Outline each Plasmodium falciparum-infected red blood cell.
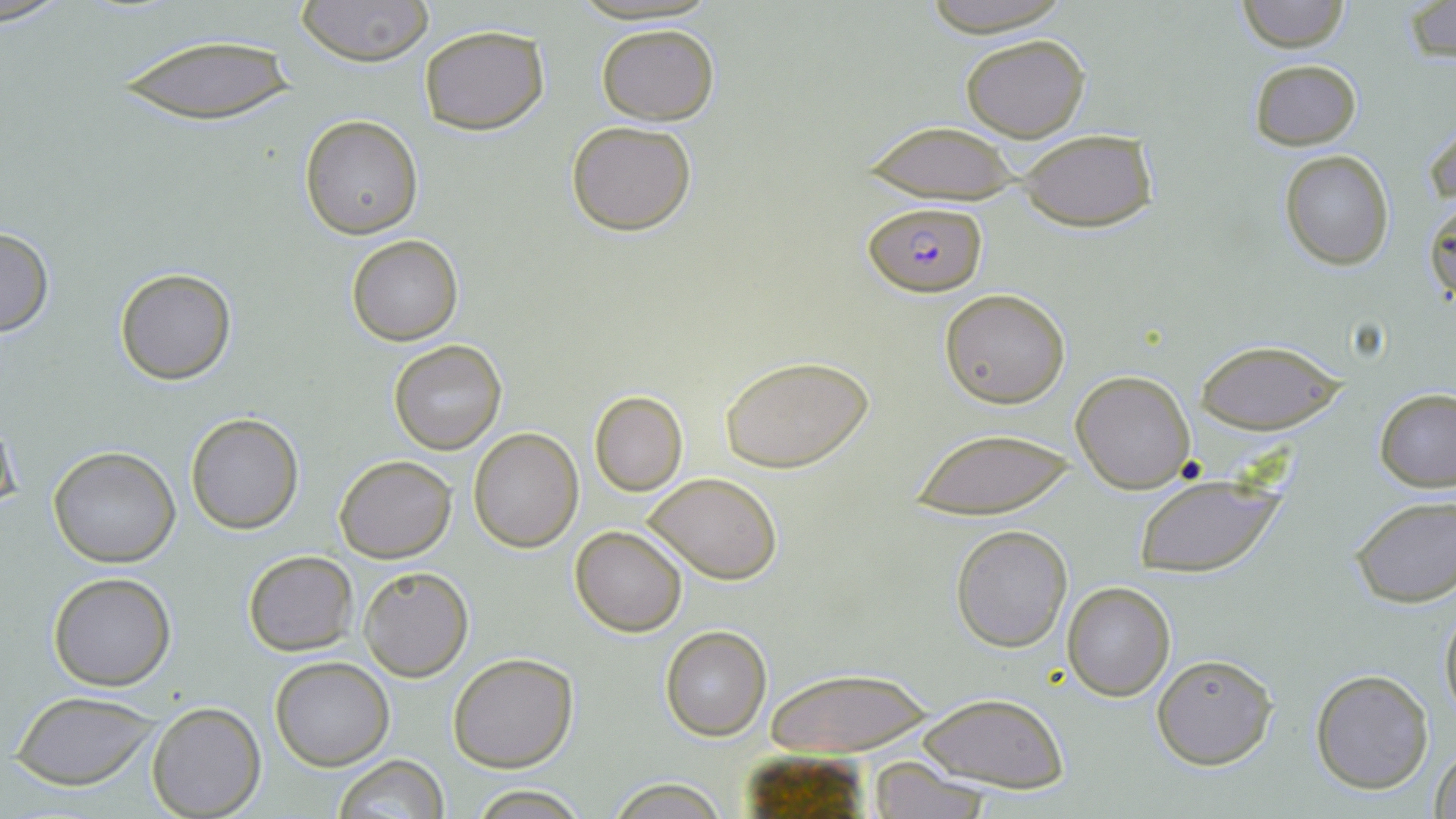

Approximate bounding boxes as (x1, y1, x2, y2) in pixels.
Plasmodium falciparum-infected red blood cells: (864, 200, 985, 295).

Summary:
  - Uninfected red blood cell locations: (295, 0, 432, 66), (1235, 0, 1351, 52), (916, 1, 1074, 35), (1404, 2, 1455, 62), (596, 23, 721, 125), (419, 25, 549, 133), (959, 32, 1093, 142), (116, 34, 300, 124), (1249, 58, 1361, 150), (300, 114, 423, 239), (1425, 120, 1455, 208), (566, 121, 697, 236), (862, 121, 1020, 202), (1015, 129, 1159, 232), (1280, 149, 1396, 271), (1425, 198, 1455, 311), (0, 227, 53, 339), (347, 236, 462, 346), (114, 268, 235, 385), (939, 288, 1071, 408), (388, 340, 506, 454), (1194, 340, 1344, 435), (719, 353, 875, 474), (1071, 370, 1195, 492), (1374, 388, 1456, 492), (590, 391, 688, 495), (0, 411, 21, 521), (185, 412, 303, 534), (468, 427, 583, 551), (906, 428, 1078, 518), (48, 445, 181, 568), (334, 454, 456, 563), (646, 472, 783, 584), (1132, 472, 1285, 579), (1349, 496, 1456, 608), (951, 524, 1072, 651), (571, 526, 687, 637), (243, 550, 356, 656), (358, 566, 473, 681), (47, 571, 177, 692), (1062, 582, 1176, 701), (1439, 593, 1456, 726), (660, 625, 772, 742), (448, 652, 578, 772), (1150, 652, 1276, 771), (270, 656, 395, 770), (767, 669, 933, 756), (1309, 669, 1433, 793), (11, 692, 160, 790), (917, 692, 1067, 792), (148, 701, 266, 818), (1430, 743, 1456, 819), (333, 753, 449, 818), (866, 757, 995, 819), (605, 778, 729, 817), (469, 787, 593, 818)
  - Slide-level diagnosis: Plasmodium falciparum
  - Image size: 1456×819 pixels
  - Field of view: one of a larger specimen
  - Preparation: thin blood smear
  - Stain: May-Grünwald-Giemsa
  - Magnification: 1000x
  - Modality: light microscopy